Assess this cell for malaria.
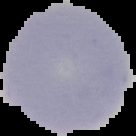

It is uninfected.

preparation: thin blood smear
image_type: segmented cell region with the area outside set to black
image_size: 136×136 pixels